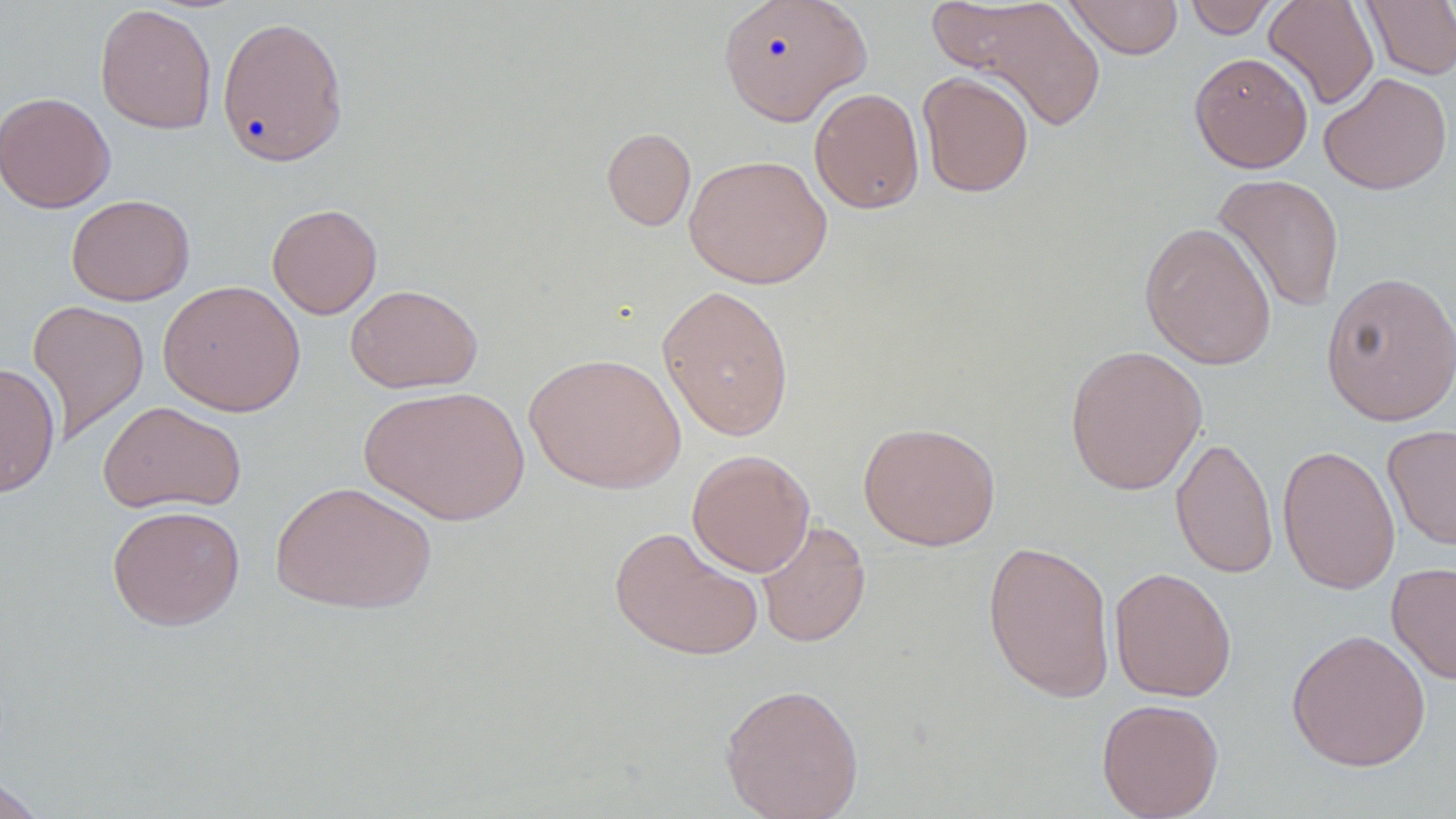

Summary:
  - Coordinate format: approximate bounding boxes as (x1,y1)-(x2,y2) corner pairs in pixels
  - Uninfected red blood cell locations: (718,0)-(872,125), (930,0)-(1108,133), (1063,0)-(1184,60), (1184,0)-(1281,39), (1263,0)-(1379,110), (1360,0)-(1456,79), (94,3)-(217,134), (216,15)-(350,167), (1189,52)-(1313,173), (916,70)-(1034,198), (1319,72)-(1453,195), (809,87)-(924,214), (0,91)-(115,213), (601,127)-(696,231), (684,154)-(833,289), (1211,173)-(1345,313), (66,194)-(195,306), (267,203)-(383,319), (1139,221)-(1277,370), (1320,271)-(1456,427), (157,279)-(306,417), (345,284)-(483,394), (657,284)-(795,441), (27,299)-(150,445), (1064,344)-(1207,496), (524,351)-(686,494), (0,362)-(61,498), (359,385)-(529,526), (99,400)-(246,515), (858,421)-(1001,550), (1382,424)-(1456,551), (1171,435)-(1279,579), (1277,444)-(1401,595), (687,449)-(815,577), (270,479)-(438,615), (106,504)-(246,631), (756,519)-(871,649), (609,525)-(764,661), (981,539)-(1117,704), (1387,561)-(1456,684), (1109,567)-(1237,702), (1286,628)-(1432,772), (719,681)-(865,819), (1096,697)-(1224,819), (0,773)-(45,819)
  - Slide-level diagnosis: no evidence of blood parasites
  - Magnification: 1000x
  - Field of view: one of a larger specimen
  - Modality: light microscopy
  - Stain: May-Grünwald-Giemsa
  - Image size: 1456×819 pixels
  - Preparation: thin blood film